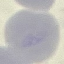

Summary:
  - Malaria status: uninfected
  - Preparation: thin smear
  - Stain: Giemsa
  - Capture: smartphone camera at the microscope eyepiece
  - Image type: cell patch, automatically extracted from a larger field of view and resized to 64 × 64 pixels